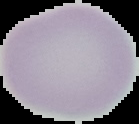

Summary:
  - Image size: 139×124 pixels
  - Result: no malaria parasites seen
  - Preparation: thin blood film
  - Image type: cell region segmented out of the field of view; surrounding area masked to black